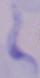 Photomicrograph. Captured at 1000x magnification. A trypanosome is shown.